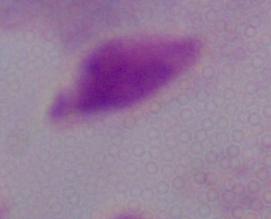
A trichomonad is seen. Photomicrograph. 1000x magnification.